Give the extent of all Plasmodium malariae-infected red blood cells.
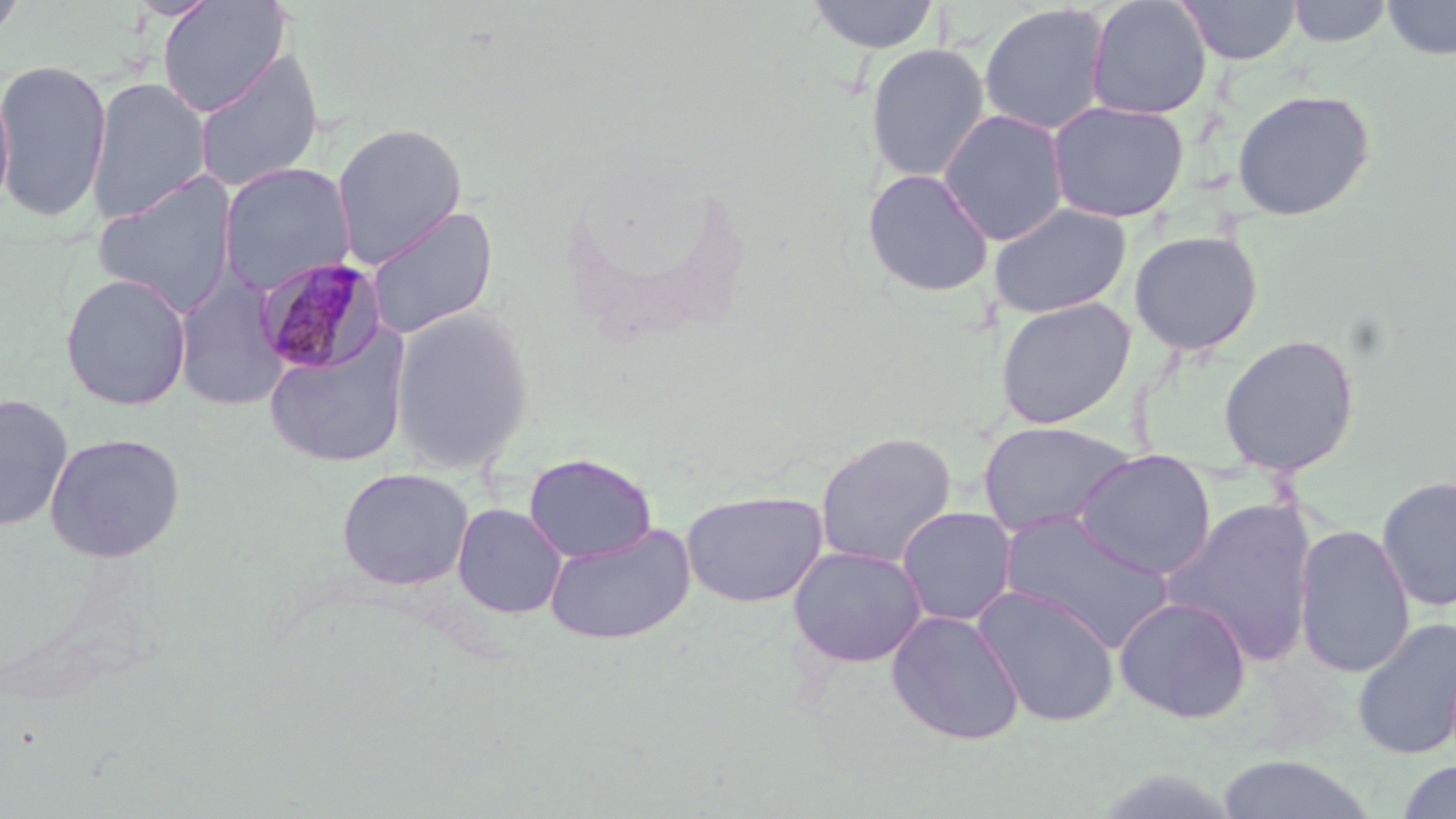

Approximate bounding boxes as (x1,y1)-(x2,y2) corner pairs in pixels.
Plasmodium malariae-infected red blood cells: (254,255)-(387,376).

Summary:
  - Uninfected red blood cell locations: (0,0)-(30,45), (156,0)-(290,116), (806,0)-(941,54), (1085,0)-(1213,119), (1178,0)-(1301,65), (1287,0)-(1393,47), (1383,0)-(1456,60), (978,3)-(1111,136), (865,43)-(991,182), (193,49)-(325,194), (0,57)-(111,222), (86,76)-(212,224), (0,78)-(16,218), (1232,89)-(1376,221), (1047,100)-(1189,223), (938,109)-(1069,245), (331,122)-(467,267), (217,163)-(355,294), (861,168)-(995,297), (91,170)-(239,316), (988,202)-(1132,319), (365,204)-(498,340), (1128,229)-(1264,356), (59,272)-(193,411), (174,272)-(291,411), (995,297)-(1136,430), (388,306)-(536,476), (263,328)-(410,469), (1218,333)-(1360,476), (0,392)-(74,531), (976,420)-(1137,539), (44,431)-(186,563), (815,431)-(958,567), (1074,449)-(1216,580), (524,452)-(657,563), (336,467)-(474,591), (1376,474)-(1456,613), (680,489)-(828,608), (1163,497)-(1319,665), (452,503)-(567,619), (896,506)-(1018,627), (997,509)-(1175,653), (544,522)-(696,646), (1294,523)-(1415,679), (787,545)-(928,667), (972,585)-(1120,727), (1113,596)-(1252,724), (886,609)-(1025,745), (1351,616)-(1456,761), (1213,754)-(1379,818), (1395,760)-(1456,818)
  - Slide-level diagnosis: Plasmodium malariae
  - Modality: light microscopy
  - Stain: May-Grünwald-Giemsa
  - Magnification: 1000x
  - Image size: 1456×819 pixels
  - Field of view: one of a larger specimen
  - Preparation: thin blood smear